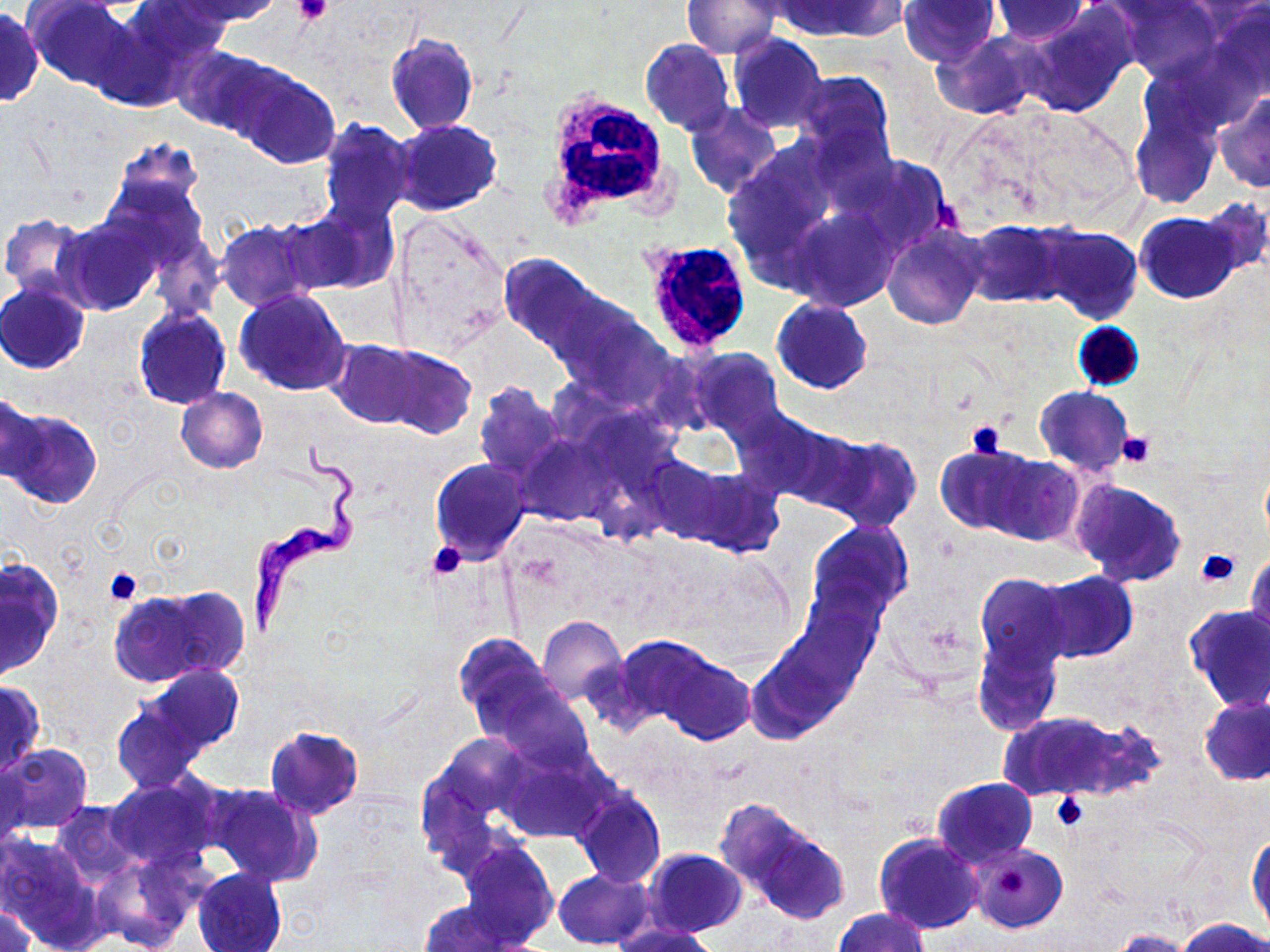
Summary:
  - Coordinate format: approximate bounding boxes as (x1, y1, x2, y2) in pixels
  - Trypanosoma brucei locations: (248, 436, 362, 639)
  - Platelet locations: (292, 0, 334, 25), (966, 420, 1008, 458), (1116, 431, 1157, 468), (428, 541, 467, 578), (1196, 547, 1240, 587), (103, 568, 142, 605), (1052, 792, 1087, 828)
  - White blood cell locations: (537, 80, 670, 226), (641, 240, 752, 354)
  - Uninfected red blood cell locations: (127, 0, 229, 73), (172, 0, 285, 26), (780, 0, 899, 39), (898, 0, 1000, 68), (25, 1, 136, 91), (681, 1, 780, 58), (1117, 1, 1221, 81), (992, 2, 1089, 41), (1207, 2, 1270, 103), (0, 7, 42, 107), (1021, 9, 1136, 118), (86, 17, 189, 111), (937, 30, 1047, 121), (385, 32, 479, 134), (727, 34, 826, 132), (639, 38, 735, 135), (175, 46, 281, 137), (233, 66, 340, 169), (791, 71, 895, 166), (1212, 93, 1270, 193), (1130, 100, 1221, 210), (685, 101, 782, 200), (319, 118, 415, 227), (393, 120, 502, 217), (106, 137, 206, 227), (839, 150, 954, 257), (1200, 197, 1270, 278), (287, 199, 397, 295), (789, 207, 901, 311), (387, 211, 512, 356), (1137, 211, 1240, 303), (0, 212, 94, 302), (58, 217, 160, 315), (963, 219, 1066, 307), (217, 220, 318, 312), (1036, 225, 1142, 323), (883, 226, 984, 329), (499, 253, 607, 362), (0, 282, 89, 374), (234, 290, 351, 396), (771, 299, 872, 393), (133, 306, 231, 409), (566, 309, 674, 410), (328, 340, 423, 426), (374, 345, 477, 439), (687, 347, 783, 440), (474, 382, 567, 482), (176, 387, 267, 472), (1035, 387, 1132, 475), (1, 390, 44, 487), (3, 409, 102, 511), (727, 409, 833, 503), (811, 433, 922, 533), (515, 434, 609, 526), (936, 445, 1033, 535), (986, 453, 1083, 545), (640, 454, 734, 543), (430, 459, 530, 564), (673, 469, 783, 556), (1071, 480, 1186, 586), (808, 521, 914, 617), (1247, 551, 1270, 647), (1, 562, 62, 677), (1035, 572, 1137, 663), (975, 573, 1072, 673), (798, 583, 885, 678), (155, 586, 249, 679), (109, 589, 220, 686), (1184, 605, 1270, 712), (537, 616, 626, 703), (453, 632, 553, 724), (610, 635, 718, 728), (972, 637, 1062, 735), (746, 651, 839, 741), (659, 653, 754, 746), (139, 664, 246, 756), (0, 680, 44, 780), (484, 681, 594, 772), (1199, 694, 1270, 786), (112, 704, 204, 792), (1002, 712, 1122, 800), (266, 725, 363, 818), (438, 733, 532, 820), (0, 745, 91, 835), (498, 748, 613, 843), (0, 756, 30, 852), (415, 763, 517, 887), (106, 777, 221, 870), (933, 777, 1037, 868), (204, 783, 320, 887), (574, 789, 666, 887), (714, 798, 825, 909), (51, 800, 140, 884), (741, 822, 849, 926), (1247, 831, 1268, 942), (0, 832, 103, 947), (875, 833, 983, 934), (459, 841, 558, 947), (970, 844, 1067, 932), (643, 849, 746, 936), (93, 854, 197, 951), (553, 868, 654, 949), (192, 869, 287, 952), (418, 901, 530, 951), (1, 904, 38, 952), (835, 907, 927, 952), (1177, 918, 1268, 952), (615, 922, 721, 951), (1110, 929, 1198, 952)
  - Slide-level diagnosis: Trypanosoma brucei
  - Image size: 1270×952 pixels
  - Modality: light microscopy
  - Preparation: thin blood smear
  - Field of view: one of a larger specimen
  - Stain: May-Grünwald-Giemsa
  - Magnification: 1000x